Locate every Plasmodium parasite.
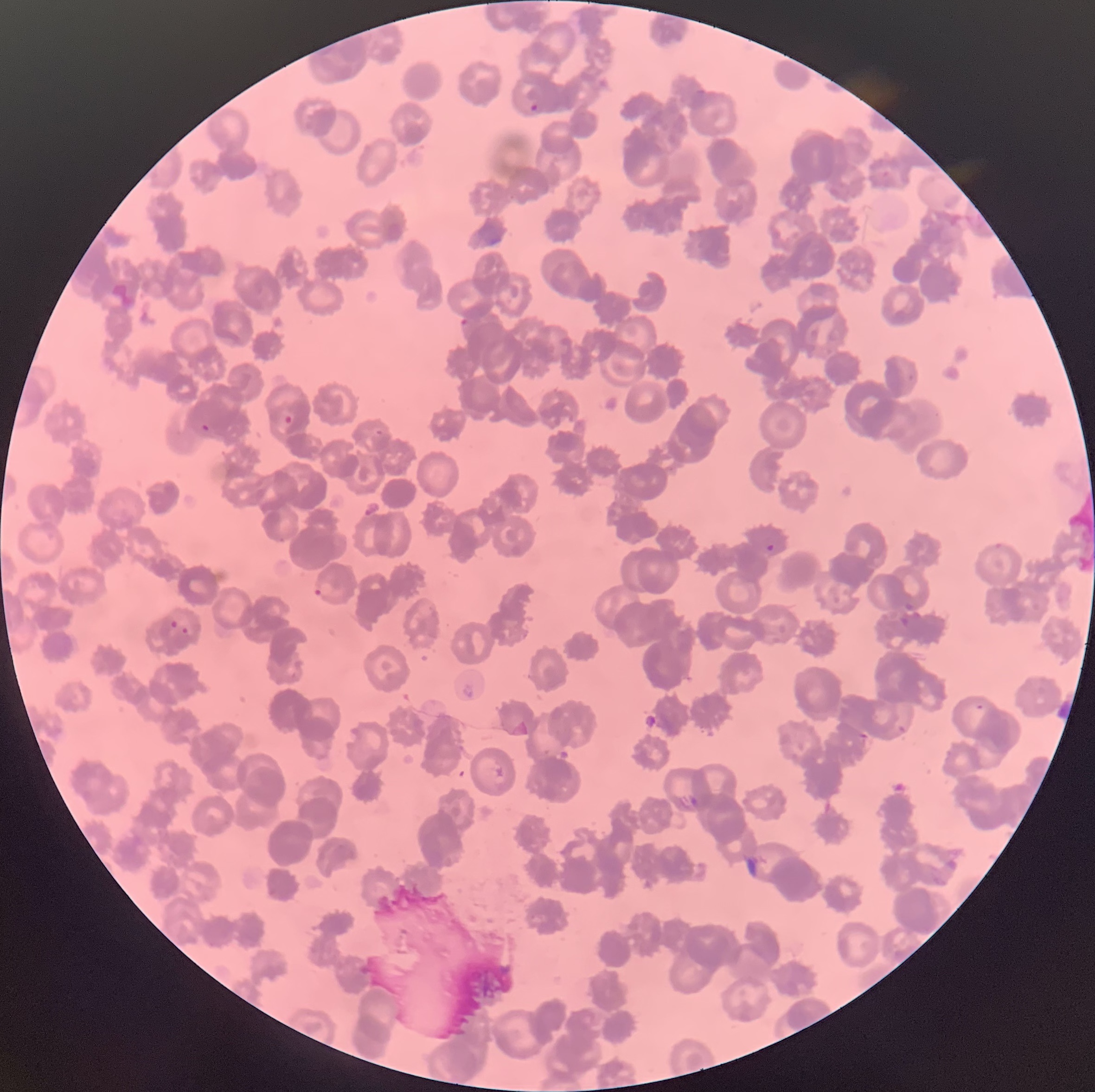

Approximate bounding boxes as [x1, y1, x2, y2] in pixels.
Plasmodium parasites: [528, 103, 541, 112], [459, 317, 470, 326], [283, 414, 293, 425], [201, 423, 210, 432], [374, 426, 386, 437], [765, 543, 776, 552], [315, 582, 339, 597], [169, 618, 179, 629], [181, 625, 190, 636], [678, 795, 700, 809].

Summary:
  - Image size: 1095×1092 pixels
  - Preparation: thin blood smear
  - Modality: light microscopy
  - Red blood cell morphology: rouleaux formation